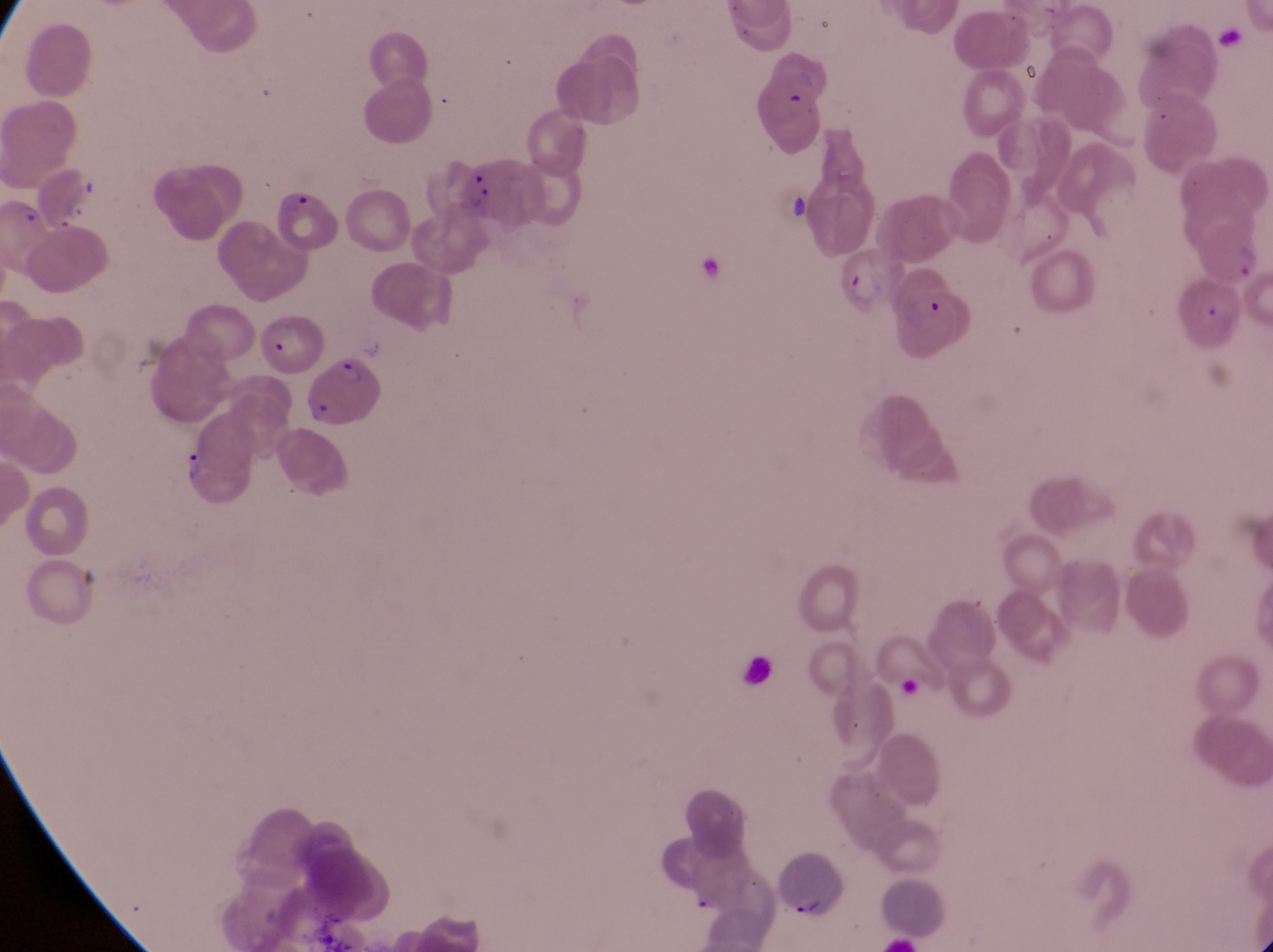

Approximate bounding boxes as [left, top, right, bottom] in pixels. Parasitised red blood cell locations: [459, 155, 546, 227], [30, 162, 104, 225], [270, 190, 339, 253], [841, 242, 904, 314], [889, 283, 976, 361], [260, 313, 322, 375], [307, 357, 385, 429], [778, 841, 850, 919]. Trophozoite locations: [178, 447, 206, 489]. Artifact (platelet-like body, stain precipitate, or debris) locations: [776, 188, 811, 231]. Collected in Uganda. Single field of view. Photographed through the eyepiece of an Olympus CX-23 microscope with a smartphone camera. Magnification of 1000x. Image is 1273×952 pixels. Thin blood smear.